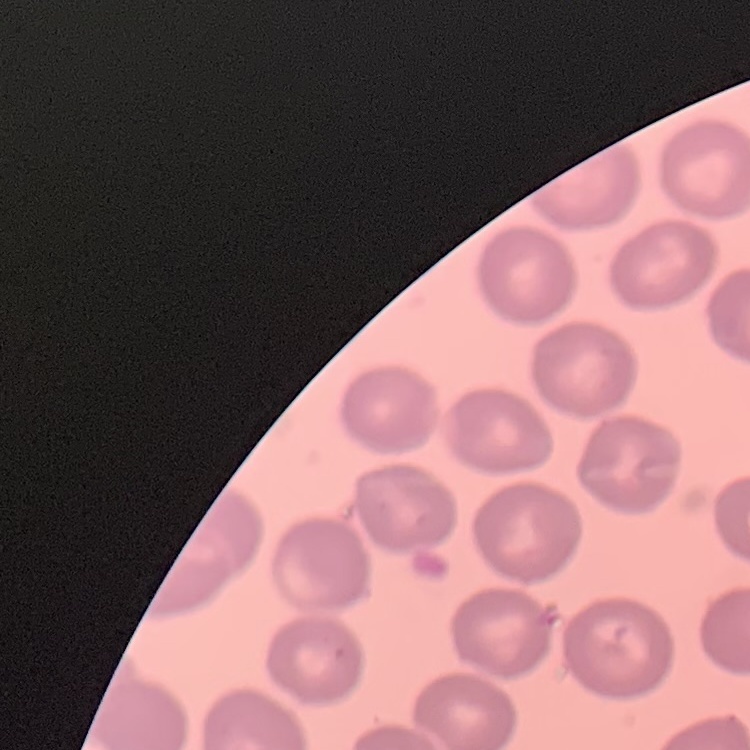
Summary:
  - Red blood cell morphology: no rouleaux formation
  - Stain: Field's or Giemsa
  - Image type: square crop of a larger photomicrograph
  - Preparation: thin blood smear